Locate every Plasmodium ovale-infected red blood cell.
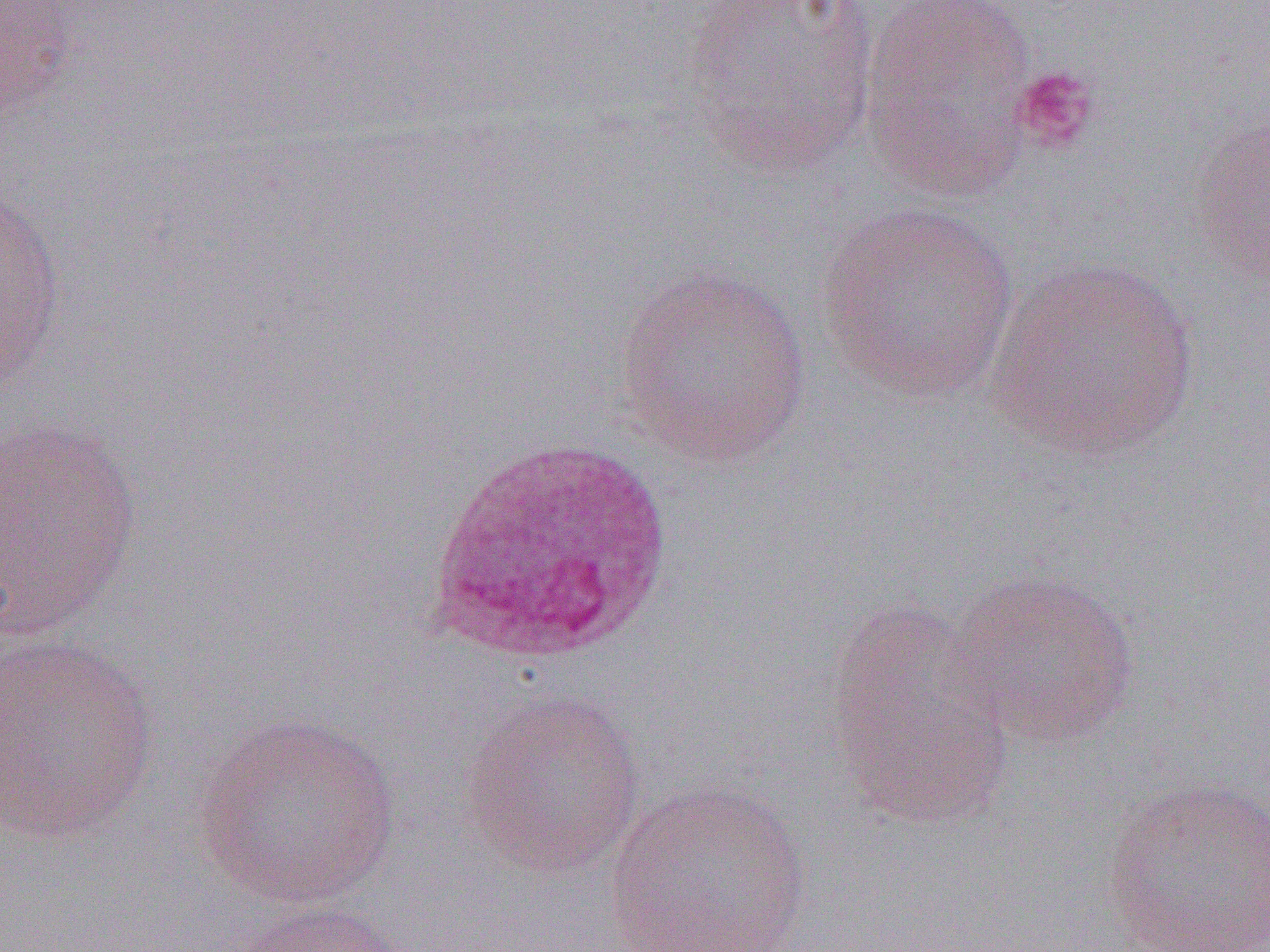
Approximate bounding boxes as (x1, y1, x2, y2) in pixels.
Plasmodium ovale-infected red blood cells: (424, 438, 677, 665).

slide-level diagnosis = Plasmodium ovale
preparation = thin blood film
image size = 1270×952 pixels
uninfected red blood cell locations = approximate bounding boxes as (x1, y1, x2, y2) in pixels: (0, 0, 81, 123), (679, 0, 881, 179), (859, 0, 1038, 199), (1187, 111, 1269, 285), (0, 183, 67, 393), (814, 201, 1020, 404), (984, 254, 1200, 462), (612, 264, 813, 468), (0, 416, 143, 641), (949, 569, 1141, 747), (825, 599, 1016, 830), (0, 634, 160, 845), (458, 687, 648, 879), (193, 712, 401, 910), (1100, 776, 1270, 951), (603, 779, 813, 951), (225, 898, 408, 952)
platelet locations = approximate bounding boxes as (x1, y1, x2, y2) in pixels: (1011, 65, 1101, 155)
magnification = 1000x
field of view = single
modality = light microscopy